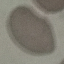

Summary:
  - Result: no malaria parasites detected
  - Stain: Giemsa
  - Image type: automatically extracted cell patch, resized to 64 × 64 pixels
  - Preparation: thin blood smear
  - Capture: smartphone through the microscope eyepiece